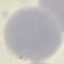

Summary:
  - Result: no malaria parasites seen
  - Preparation: thin smear
  - Image type: automatically extracted cell patch, resized to 64 × 64 pixels
  - Capture: smartphone camera at the microscope eyepiece
  - Stain: Giemsa